Give the preparation type.
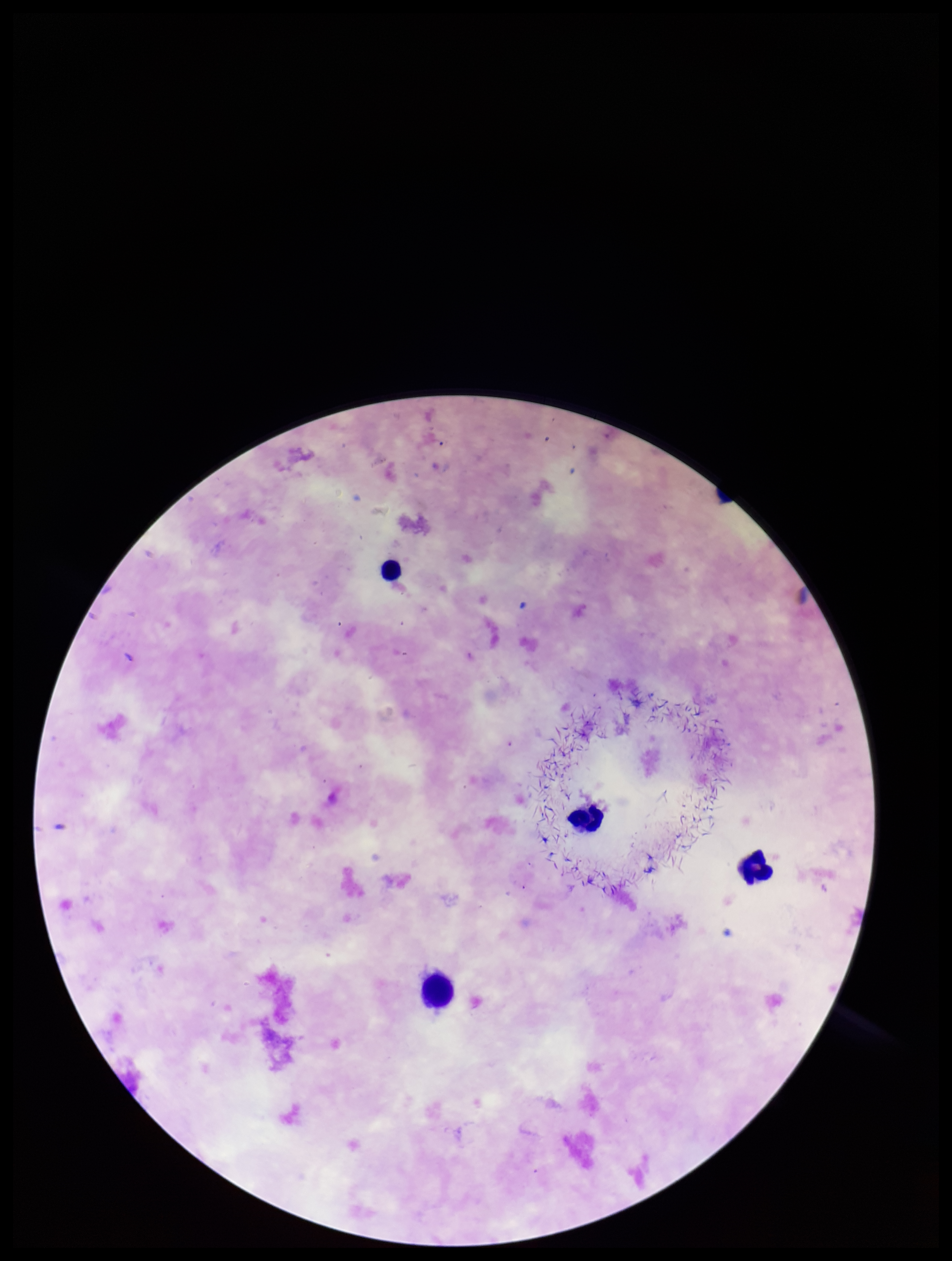

Thick.

{
  "image_size": "952×1261 pixels",
  "species_reported_for_this_patient": "Plasmodium falciparum",
  "parasite_count": 0,
  "stain": "Giemsa",
  "patient_malaria_status": "positive",
  "field_of_view": "single",
  "leukocyte_count": 3,
  "capture": "smartphone photograph through the microscope eyepiece",
  "plasmodium_parasites": "none seen"
}